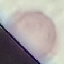
{
  "malaria_status": "uninfected",
  "stain": "Giemsa",
  "preparation": "thin blood film",
  "image_type": "automatically extracted cell patch, resized to 64 × 64 pixels",
  "capture": "smartphone through the microscope eyepiece"
}